Name the cell type shown.
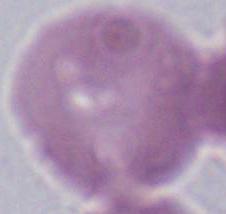
This is an erythrocyte.

Summary:
  - Modality: micrograph
  - Magnification: 1000x